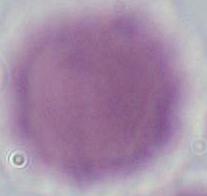
Summary:
  - Modality: micrograph
  - Identification: red blood cell
  - Magnification: 1000x